Report the malaria status of this cell.
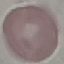
It is uninfected.

Thin smear of blood. Automatically extracted cell patch, resized to 64 × 64 pixels. Giemsa stain. Photographed with a smartphone camera at the microscope eyepiece.